Comment on the morphology of the red blood cells.
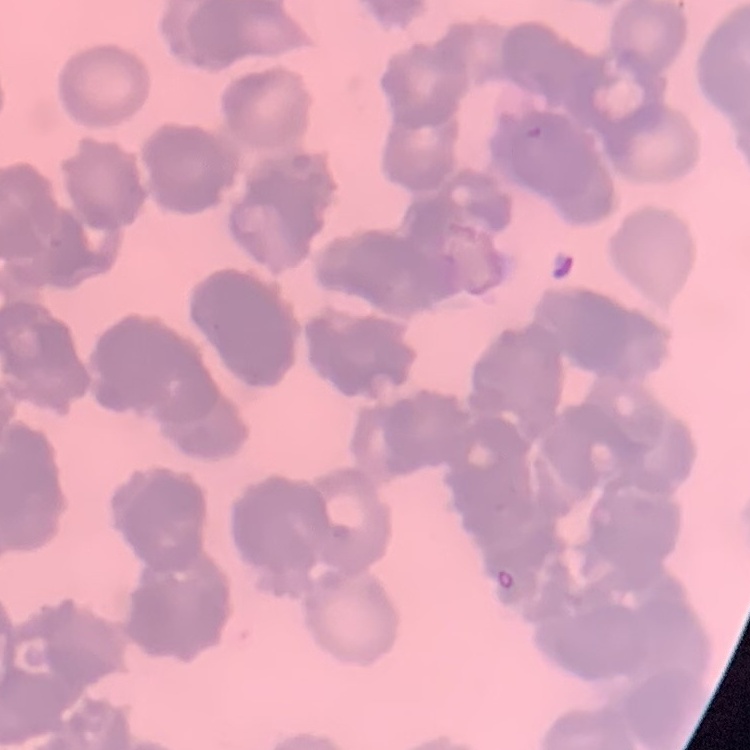
They show rouleaux formation.

Summary:
  - Image type: square crop of a larger photomicrograph
  - Preparation: thin blood smear
  - Stain: Field's or Giemsa